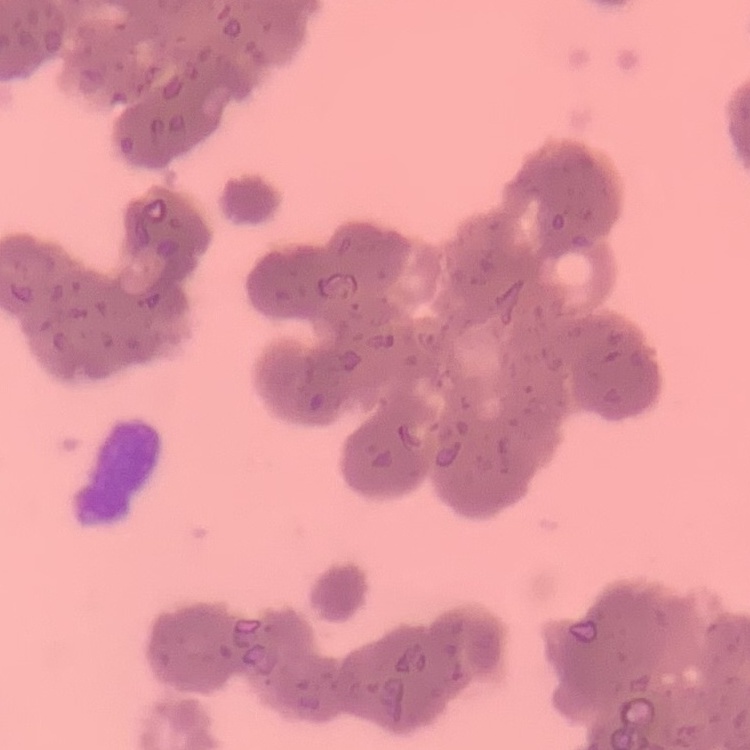

erythrocyte morphology = rouleaux formation
stain = Field's or Giemsa
image type = square crop of a larger photomicrograph
preparation = thin peripheral smear